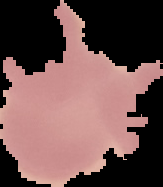
From a thin blood film. Image is 163×187 pixels. The area outside the segmented cell region is set to black. Malaria status: uninfected.